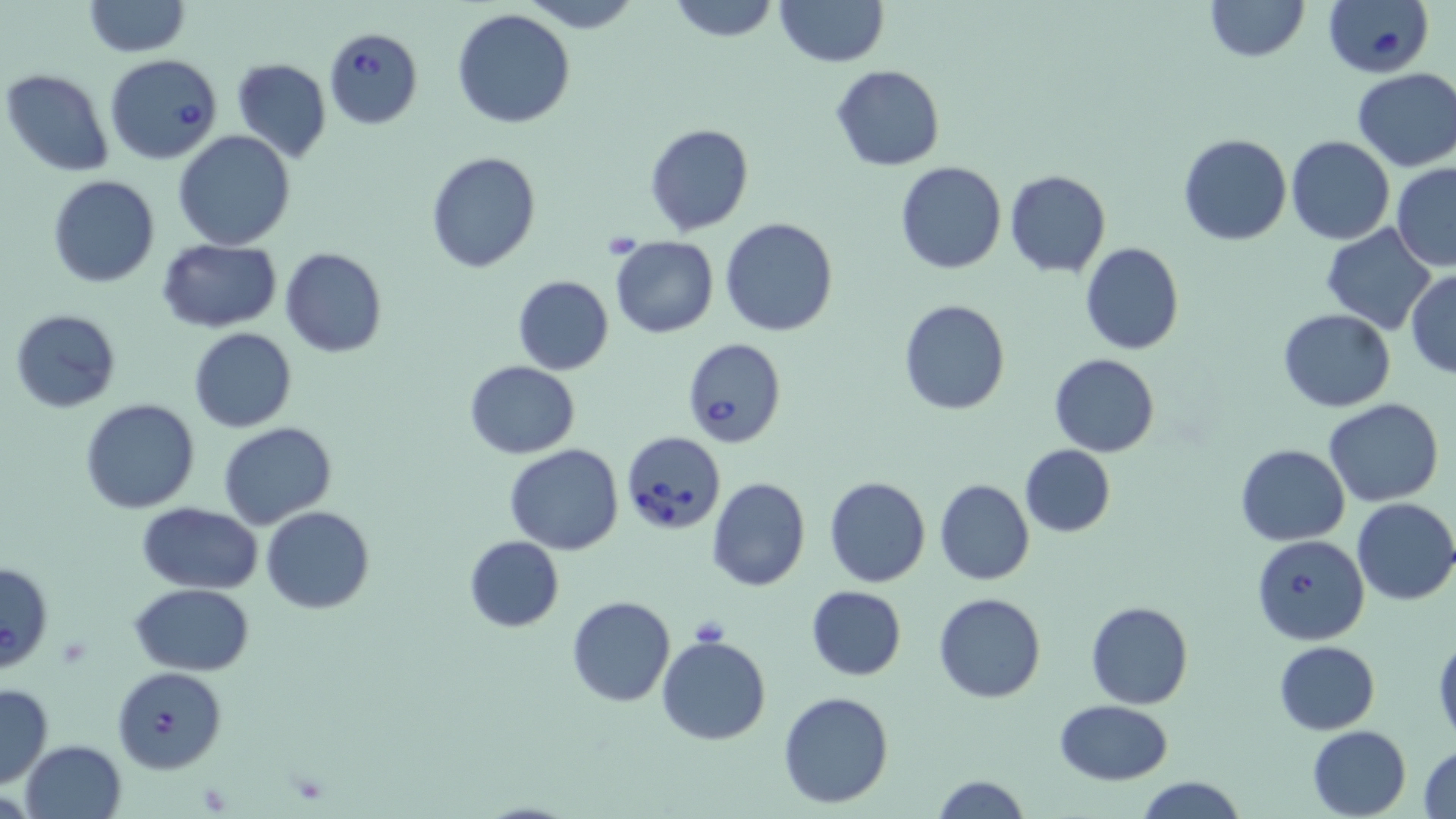

Summary:
  - Coordinate format: approximate bounding boxes as named x1/y1/x2/y2 corners in pixels
  - Babesia divergens-infected red blood cell locations: (x1=1323, y1=0, x2=1436, y2=77), (x1=324, y1=28, x2=422, y2=130), (x1=106, y1=55, x2=224, y2=165), (x1=682, y1=338, x2=785, y2=448), (x1=621, y1=430, x2=725, y2=535), (x1=1251, y1=533, x2=1369, y2=644), (x1=0, y1=560, x2=54, y2=673), (x1=112, y1=667, x2=225, y2=774)
  - Uninfected red blood cell locations: (x1=518, y1=0, x2=643, y2=33), (x1=665, y1=0, x2=780, y2=42), (x1=774, y1=0, x2=889, y2=67), (x1=1205, y1=0, x2=1308, y2=62), (x1=82, y1=1, x2=189, y2=57), (x1=452, y1=9, x2=576, y2=129), (x1=231, y1=57, x2=331, y2=162), (x1=830, y1=65, x2=945, y2=170), (x1=1352, y1=68, x2=1456, y2=171), (x1=2, y1=69, x2=114, y2=177), (x1=644, y1=123, x2=753, y2=234), (x1=173, y1=130, x2=295, y2=250), (x1=1177, y1=133, x2=1291, y2=245), (x1=1286, y1=136, x2=1394, y2=245), (x1=425, y1=152, x2=542, y2=274), (x1=895, y1=161, x2=1006, y2=274), (x1=1394, y1=163, x2=1456, y2=270), (x1=1005, y1=170, x2=1111, y2=277), (x1=48, y1=176, x2=160, y2=288), (x1=720, y1=217, x2=839, y2=337), (x1=1321, y1=223, x2=1437, y2=334), (x1=610, y1=236, x2=719, y2=338), (x1=157, y1=239, x2=282, y2=332), (x1=1080, y1=241, x2=1184, y2=355), (x1=280, y1=248, x2=387, y2=359), (x1=1406, y1=269, x2=1456, y2=377), (x1=511, y1=275, x2=615, y2=374), (x1=898, y1=300, x2=1009, y2=416), (x1=9, y1=308, x2=121, y2=413), (x1=1279, y1=309, x2=1396, y2=412), (x1=188, y1=327, x2=297, y2=432), (x1=1049, y1=354, x2=1160, y2=457), (x1=465, y1=360, x2=580, y2=458), (x1=80, y1=398, x2=200, y2=513), (x1=1324, y1=398, x2=1445, y2=507), (x1=218, y1=422, x2=339, y2=531), (x1=505, y1=443, x2=624, y2=556), (x1=1019, y1=444, x2=1117, y2=537), (x1=1234, y1=444, x2=1351, y2=546), (x1=825, y1=476, x2=931, y2=588), (x1=708, y1=477, x2=810, y2=592), (x1=935, y1=479, x2=1035, y2=585), (x1=1352, y1=498, x2=1456, y2=606), (x1=137, y1=502, x2=262, y2=593), (x1=262, y1=507, x2=375, y2=614), (x1=463, y1=536, x2=564, y2=632), (x1=132, y1=584, x2=255, y2=674), (x1=806, y1=585, x2=908, y2=680), (x1=934, y1=593, x2=1045, y2=703), (x1=567, y1=595, x2=675, y2=706), (x1=1086, y1=600, x2=1194, y2=709), (x1=657, y1=634, x2=772, y2=746), (x1=1432, y1=634, x2=1456, y2=743), (x1=1272, y1=640, x2=1380, y2=735), (x1=0, y1=681, x2=54, y2=789), (x1=777, y1=691, x2=894, y2=809), (x1=1054, y1=700, x2=1176, y2=785), (x1=1308, y1=725, x2=1412, y2=818), (x1=20, y1=740, x2=128, y2=819), (x1=1418, y1=743, x2=1455, y2=817), (x1=1134, y1=775, x2=1248, y2=819), (x1=929, y1=776, x2=1031, y2=818)
  - Slide-level diagnosis: Babesia divergens
  - Preparation: thin blood film
  - Modality: light microscopy
  - Magnification: 1000x
  - Field of view: single
  - Image size: 1456×819 pixels
  - Stain: May-Grünwald-Giemsa